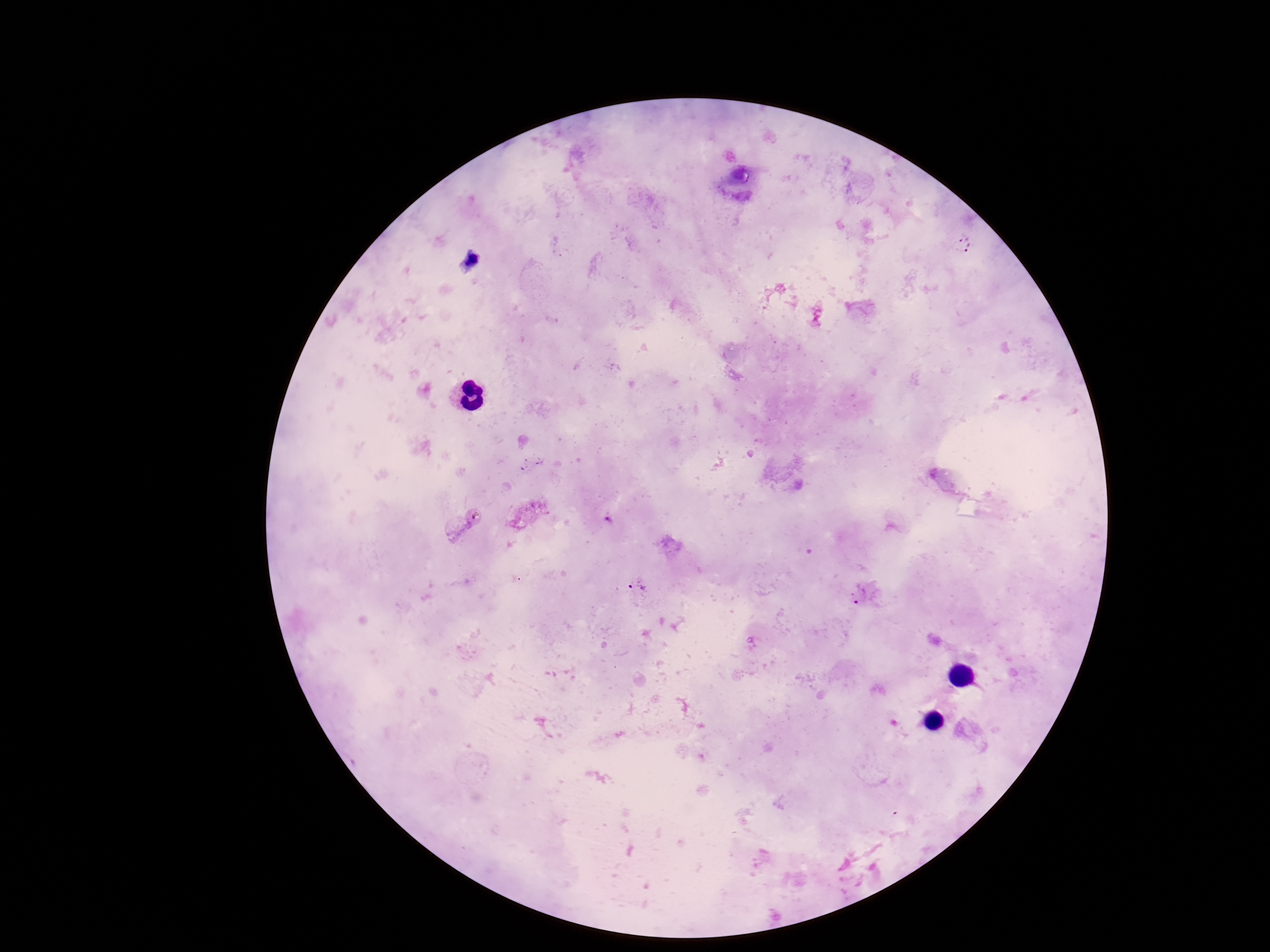
Approximate centers as {x, y} in pixels.
Summary:
  - Plasmodium parasite locations: {964, 243}, {609, 520}, {637, 585}, {862, 594}
  - Preparation: thick blood film
  - Patient malaria status: infected
  - Magnification: 100x
  - Capture: smartphone camera through the microscope eyepiece
  - Field of view: one from this slide
  - Stain: Giemsa
  - Image size: 1270×952 pixels